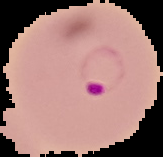
preparation = thin blood film
image size = 163×157 pixels
malaria status = parasitized
image type = cell region segmented out of the field of view; surrounding area masked to black